State the preparation type.
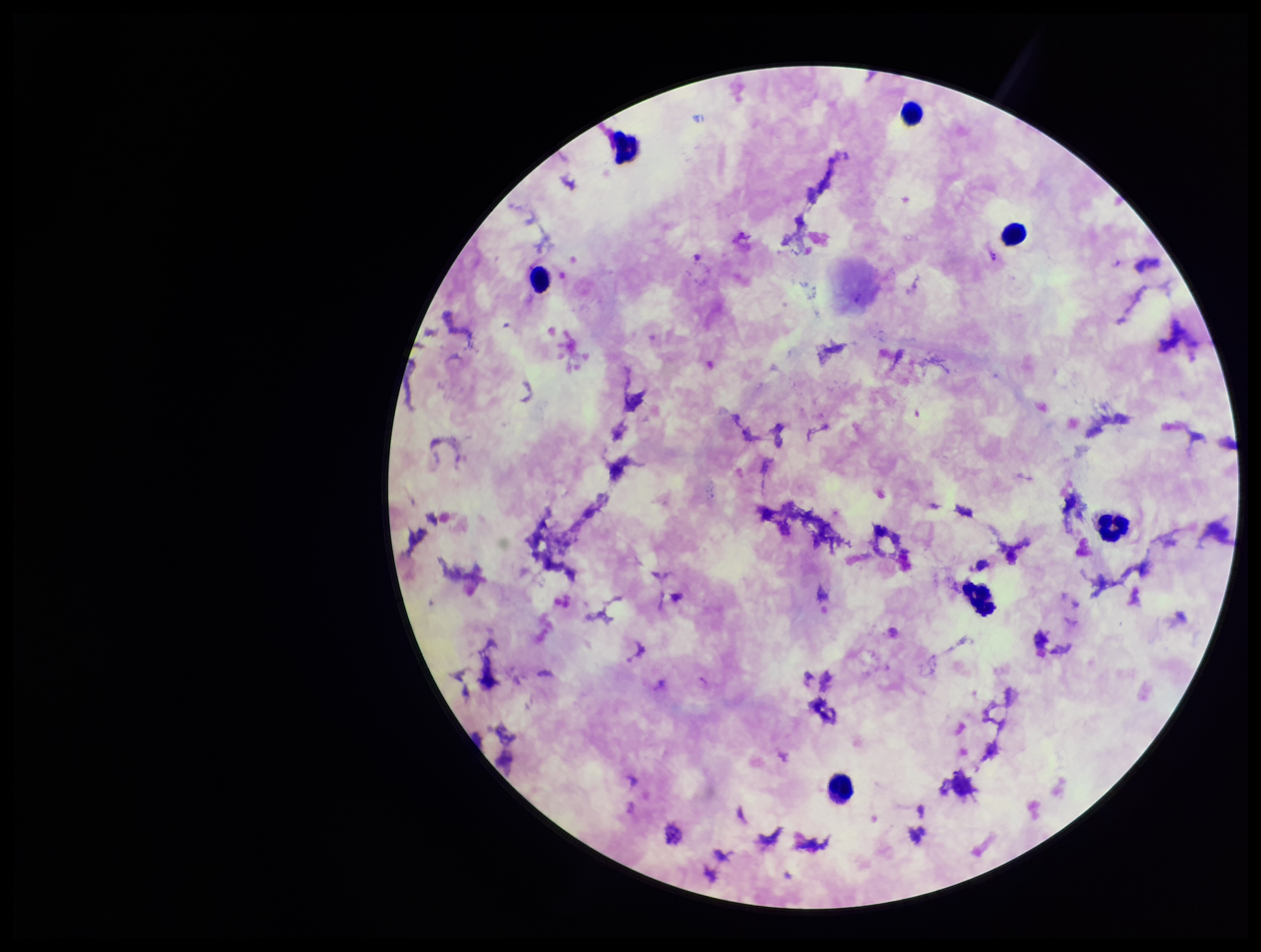

Thick.

Patient malaria status: positive. Parasite count: 0. Single field of view. Smartphone photograph taken through the eyepiece of a microscope. Plasmodium parasites: none identified. Stained with Giemsa. Leukocyte count: 7. Species reported for this patient: Plasmodium falciparum. Image is 1261×952 pixels.